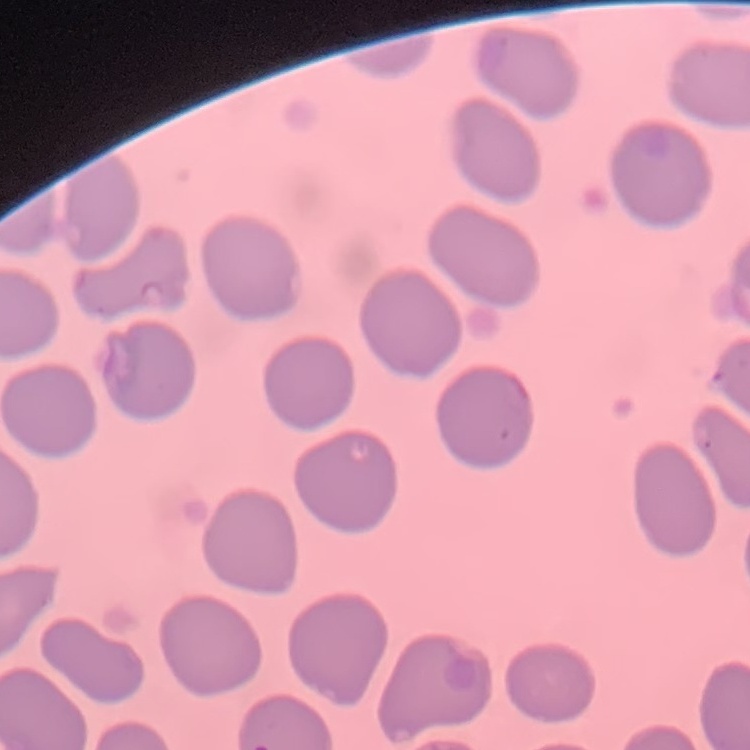

The erythrocytes exhibit no rouleaux formation. Field's or Giemsa stain. Thin peripheral smear. One tile cut from a larger photomicrograph.